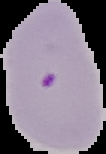

The area outside the segmented cell region is set to black. Image is 106×154 pixels. Malaria status: parasitized. From a thin blood film.